Name the blood parasite species.
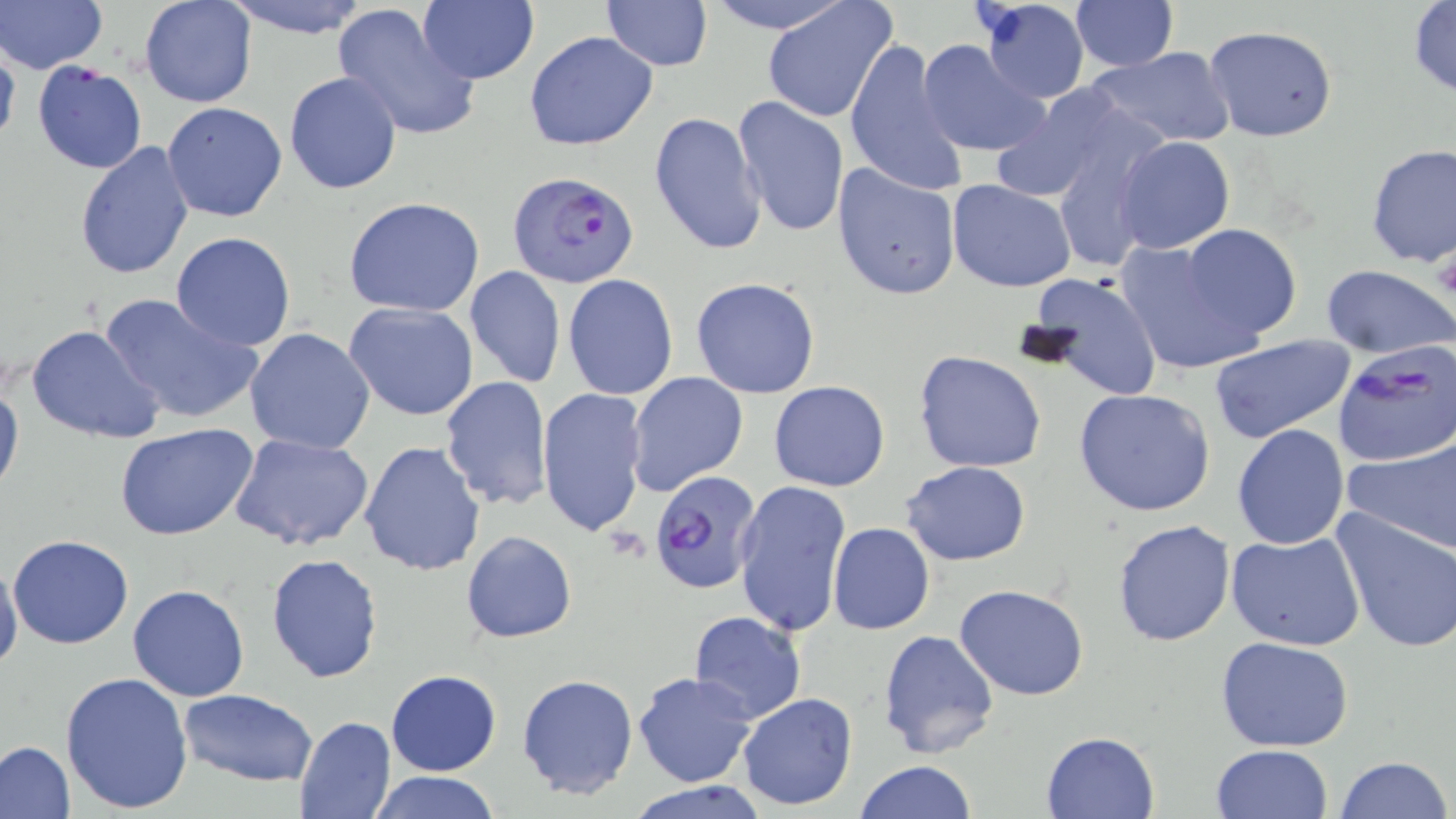

Plasmodium falciparum.

magnification = 1000x
Plasmodium falciparum-infected red blood cell locations = approximate bounding boxes as (x1, y1, x2, y2) in pixels: (507, 170, 640, 288), (1331, 341, 1456, 470), (649, 470, 762, 594)
modality = light microscopy
stain = May-Grünwald-Giemsa
image size = 1456×819 pixels
uninfected red blood cell locations = approximate bounding boxes as (x1, y1, x2, y2) in pixels: (0, 0, 107, 75), (140, 0, 257, 108), (221, 0, 373, 38), (418, 0, 539, 86), (601, 0, 713, 70), (702, 0, 855, 35), (759, 0, 896, 124), (977, 1, 1092, 102), (1069, 1, 1177, 72), (332, 2, 483, 143), (1407, 2, 1455, 100), (1203, 24, 1339, 142), (524, 31, 658, 152), (915, 37, 1051, 160), (0, 38, 21, 158), (843, 39, 968, 199), (1088, 44, 1236, 149), (30, 62, 149, 173), (284, 72, 403, 196), (988, 81, 1150, 210), (733, 97, 850, 237), (162, 101, 290, 223), (650, 108, 766, 259), (1117, 136, 1234, 253), (1055, 140, 1157, 274), (74, 142, 197, 283), (1365, 143, 1455, 268), (832, 162, 962, 300), (948, 179, 1076, 291), (343, 199, 485, 317), (1178, 223, 1302, 344), (172, 232, 295, 353), (1113, 236, 1272, 376), (1319, 263, 1455, 359), (465, 266, 566, 388), (1025, 271, 1163, 402), (563, 275, 677, 399), (690, 276, 822, 398), (99, 292, 267, 425), (344, 302, 479, 421), (24, 323, 169, 447), (244, 328, 375, 456), (1206, 334, 1356, 445), (914, 350, 1048, 474), (627, 372, 749, 498), (440, 375, 551, 511), (0, 377, 25, 504), (768, 380, 891, 492), (537, 386, 649, 540), (1074, 387, 1217, 518), (113, 421, 260, 543), (1231, 423, 1351, 549), (230, 433, 375, 553), (1345, 437, 1456, 557), (360, 440, 486, 577), (901, 461, 1030, 565), (732, 478, 852, 638), (1333, 510, 1456, 655), (1112, 519, 1235, 646), (827, 523, 934, 634), (462, 530, 577, 643), (1226, 531, 1366, 650), (5, 534, 136, 650), (265, 553, 383, 686), (0, 557, 24, 678), (127, 584, 250, 701), (954, 584, 1090, 701), (687, 611, 807, 723), (877, 629, 999, 758), (1214, 634, 1355, 751), (386, 670, 501, 776), (61, 671, 194, 814), (632, 672, 757, 788), (516, 673, 638, 798), (176, 689, 320, 787), (736, 692, 857, 811), (296, 716, 397, 819), (1041, 730, 1161, 819), (0, 740, 75, 819), (1209, 745, 1334, 819), (1335, 756, 1452, 819), (854, 760, 977, 818), (368, 770, 501, 819), (624, 779, 770, 818)
platelet locations = approximate bounding boxes as (x1, y1, x2, y2) in pixels: (1433, 253, 1456, 299), (1009, 319, 1090, 373), (601, 527, 648, 564)
preparation = thin blood film
field of view = one of a larger specimen